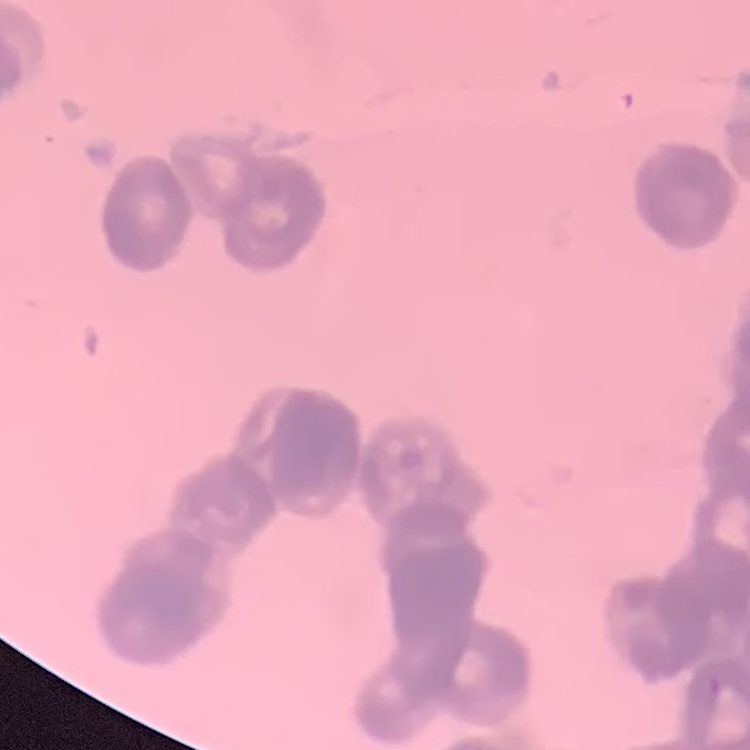
erythrocyte morphology = rouleaux formation
preparation = thin blood film
image type = square crop of a larger photomicrograph
stain = Field's or Giemsa